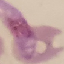

Summary:
  - Malaria status: parasitized
  - Stain: Giemsa
  - Capture: smartphone through the microscope eyepiece
  - Preparation: thin blood film
  - Image type: automatically extracted cell patch, resized to 64 × 64 pixels